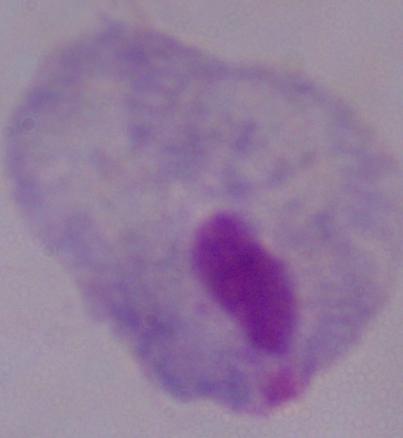

{
  "modality": "micrograph",
  "identification": "trichomonad",
  "magnification": "1000x"
}